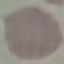
malaria status = uninfected
preparation = thin blood smear
capture = smartphone camera at the microscope eyepiece
image type = automatically extracted cell patch, resized to 64 × 64 pixels
stain = Giemsa